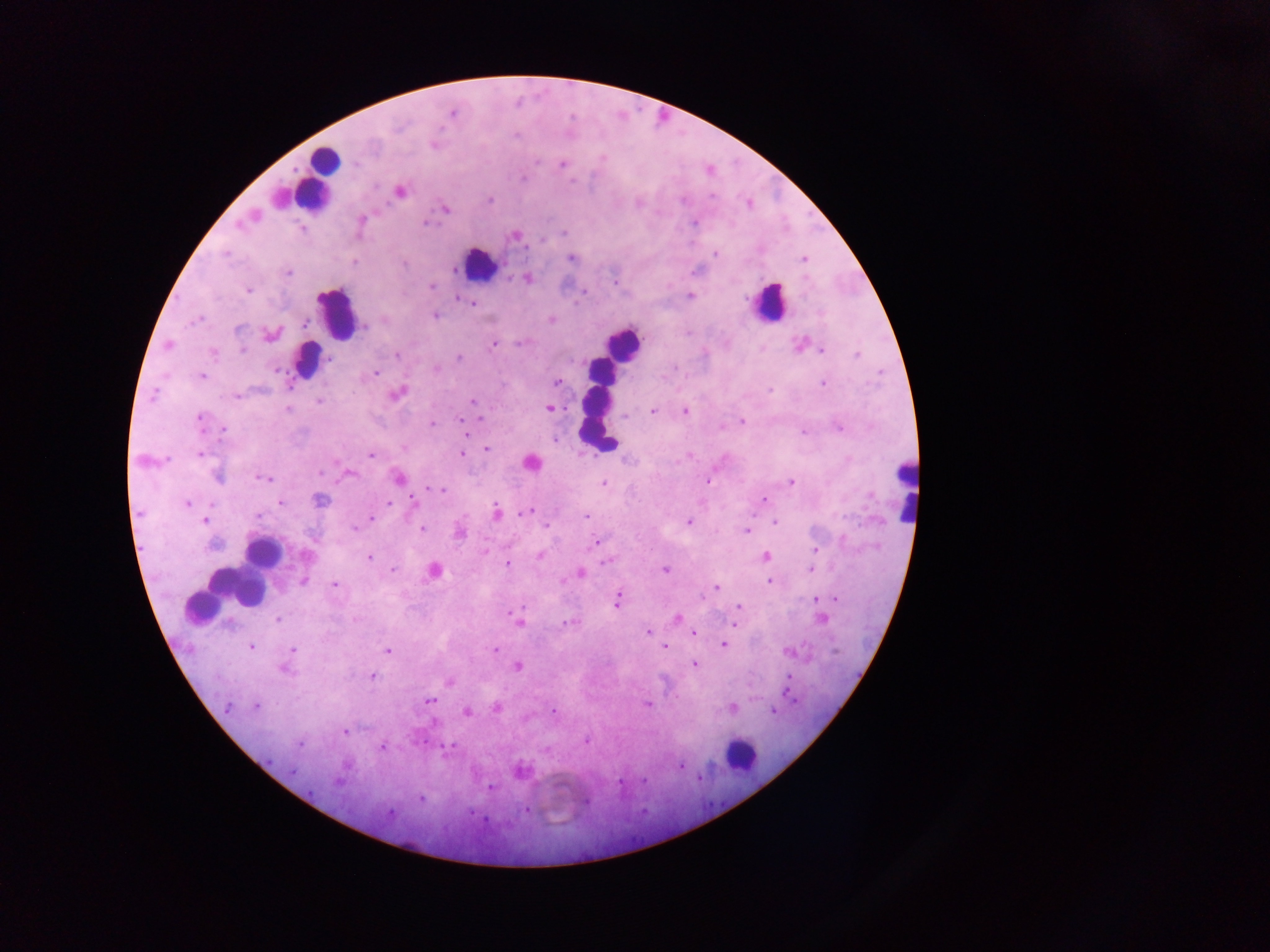

capture = mobile-phone photograph through a microscope
country = Ghana
field of view = single
preparation = thick blood smear
Plasmodium parasite locations = approximate centers as x y in pixels: 453 113; 516 135; 434 144; 603 158; 537 161; 562 164; 523 178; 400 192; 712 196; 489 199; 748 203; 446 208; 361 219; 426 223; 695 223; 239 225; 564 233; 516 236; 543 240; 715 253; 225 254; 572 258; 804 260; 354 262; 404 264; 288 272; 527 279; 614 283; 432 286; 248 289; 690 295; 457 299; 472 303; 435 316; 198 319; 552 319; 304 323; 365 327; 239 329; 271 335; 520 342; 799 344; 168 345; 493 345; 242 350; 823 351; 213 353; 396 356; 856 356; 459 357; 329 360; 275 371; 375 373; 201 376; 556 383; 823 383; 770 390; 397 394; 153 395; 235 396; 319 401; 472 402; 549 408; 287 410; 653 411; 685 412; 624 417; 199 418; 480 418; 460 420; 741 421; 431 423; 839 428; 224 431; 804 431; 466 434; 487 449; 200 453; 463 454; 371 456; 530 463; 321 473; 348 474; 218 477; 264 478; 400 479; 708 481; 790 482; 603 483; 429 489; 440 490; 413 499; 320 500; 764 500; 279 503; 388 503; 186 504; 496 512; 524 512; 585 516; 257 517; 372 518; 205 521; 689 522; 775 522; 546 525; 354 528; 421 529; 747 531; 594 543; 213 545; 815 549; 485 552; 306 555; 540 556; 766 556; 369 557; 604 562; 507 564; 392 570; 664 570; 811 570; 433 571; 581 573; 303 581; 769 582; 335 584; 717 588; 835 598; 816 599; 618 600; 739 606; 510 613; 678 618; 278 619; 823 619; 568 622; 519 623; 734 624; 647 633; 693 634; 723 644; 251 647; 665 647; 293 649; 495 650; 388 651; 787 651; 694 665; 518 666; 285 669; 372 676; 788 677; 450 683; 430 701; 647 704; 256 706; 228 707; 496 708; 732 708; 553 710; 467 712; 773 712; 434 723; 344 732; 586 741; 300 744; 382 747; 450 747; 680 766; 519 770; 293 771; 645 780; 337 782; 491 788; 421 799; 586 801; 527 810; 390 813; 484 819
leukocyte locations = approximate centers as x y in pixels: 323 157; 317 175; 479 265; 770 300; 335 314; 620 343; 307 359; 601 370; 598 414; 902 490; 262 552; 236 587; 741 754
image size = 1270×952 pixels